Describe the morphology of the erythrocytes.
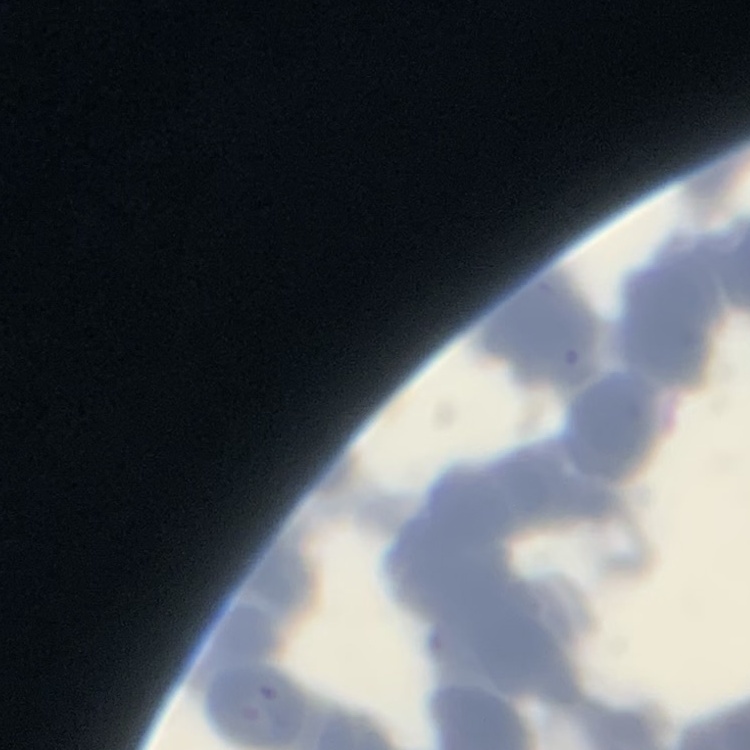
They show rouleaux formation.

Summary:
  - Stain: Field's or Giemsa
  - Image type: one tile cut from a larger photomicrograph
  - Preparation: thin blood film